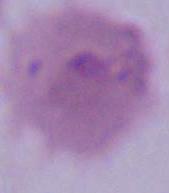
modality = photomicrograph
magnification = 1000x
identification = erythrocyte